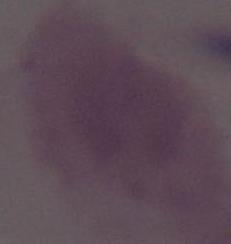 A red blood cell is shown. Micrograph. 1000x magnification.